Classify this cell by malaria status.
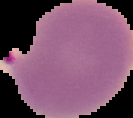

It is parasitized.

preparation = thin blood smear
image size = 133×118 pixels
image type = segmented cell region on a black background